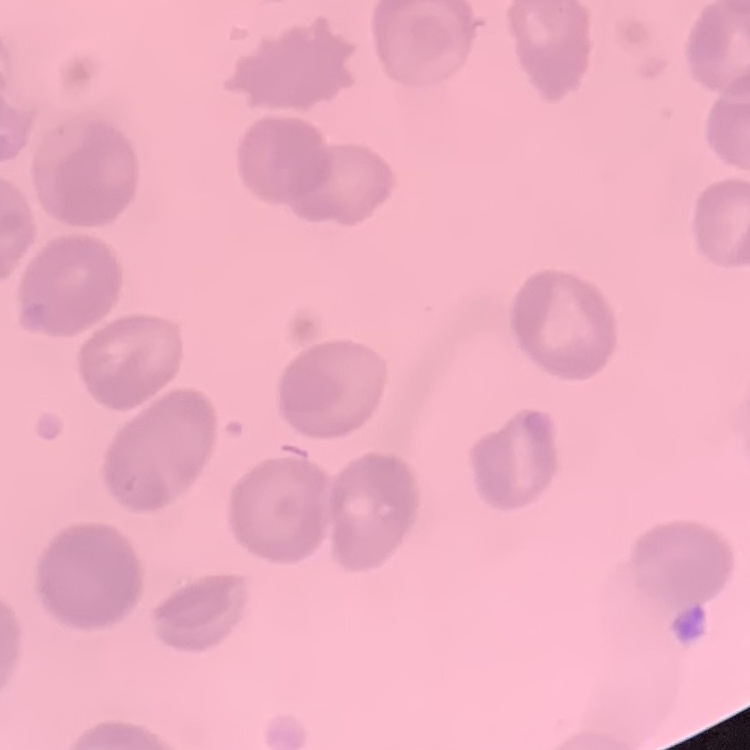
erythrocyte_morphology: no rouleaux formation
preparation: thin blood film
image_type: square crop of a larger photomicrograph
stain: Field's or Giemsa